Give the position of every leukocyte visible.
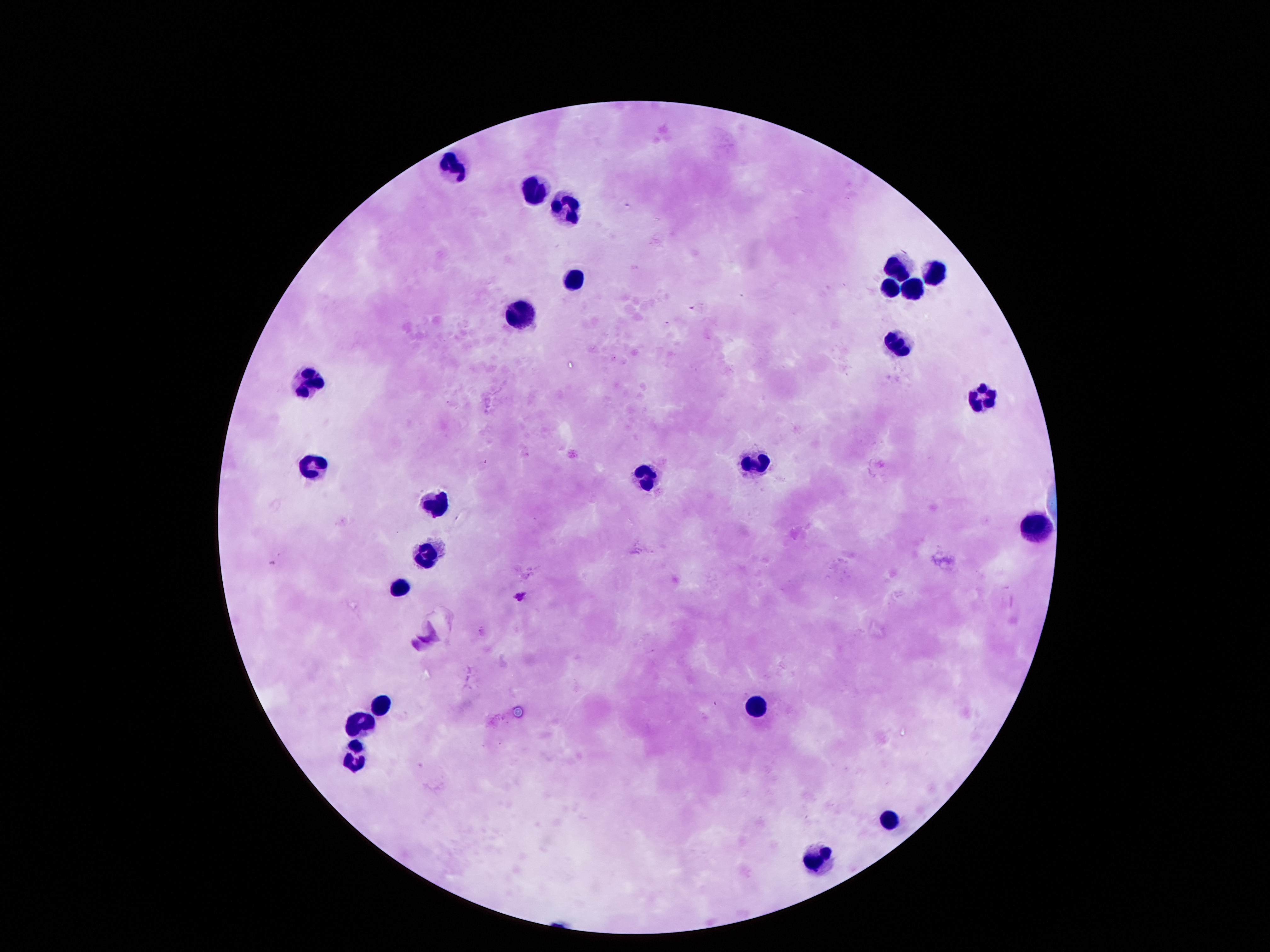
Approximate centers as [x, y] in pixels.
Leukocytes: [447, 163], [538, 189], [558, 204], [898, 268], [935, 270], [571, 278], [887, 287], [908, 288], [518, 315], [898, 342], [306, 382], [982, 399], [756, 463], [313, 466], [649, 471], [434, 502], [1029, 523], [427, 555], [397, 587], [753, 701], [376, 703], [360, 725], [353, 752], [884, 819], [817, 858].

Summary:
  - Preparation: thick peripheral-blood smear
  - Stain: Giemsa
  - Capture: smartphone camera through the microscope eyepiece
  - Magnification: 100x
  - Image size: 1270×952 pixels
  - Patient malaria status: negative
  - Field of view: one from this slide